Identify the parasite.
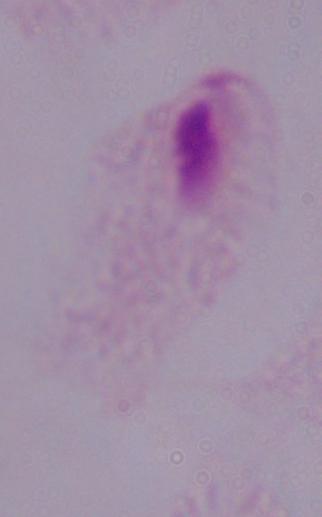
This is a trichomonad.

{
  "magnification": "1000x",
  "modality": "micrograph"
}